Name the parasite shown.
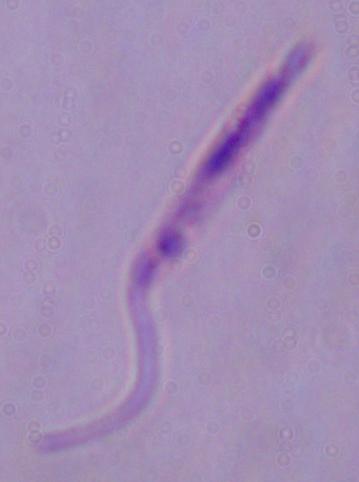
This is Leishmania.

magnification = 1000x
modality = photomicrograph